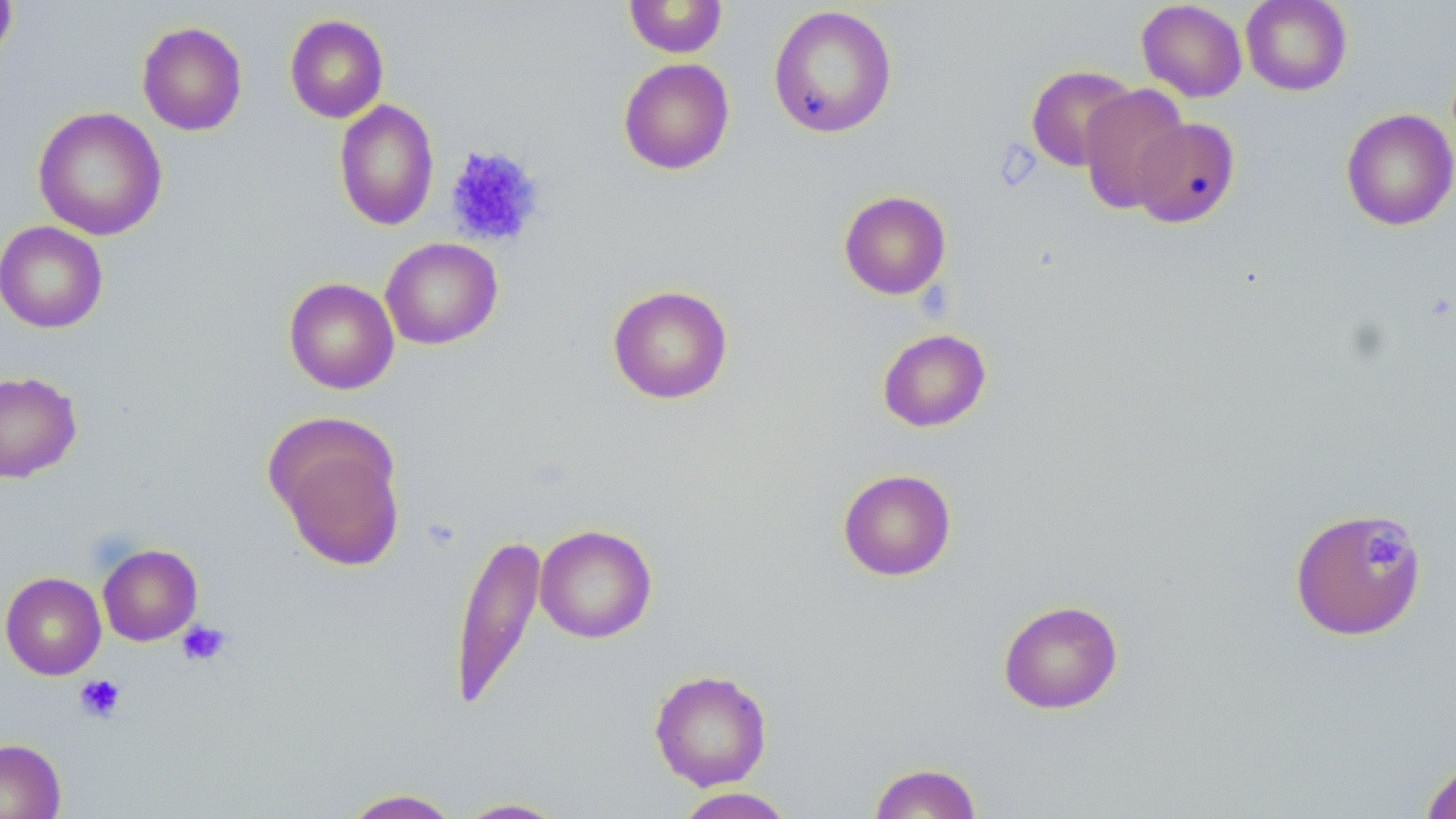 Approximate bounding boxes as (x1,y1)-(x2,y2) corner pairs in pixels. Platelet locations: (443,145)-(544,248), (1361,525)-(1409,574), (175,620)-(232,666), (75,674)-(125,723). Uninfected red blood cell locations: (0,0)-(18,63), (1241,0)-(1352,96), (624,1)-(728,58), (1136,1)-(1248,102), (768,5)-(897,138), (284,14)-(388,123), (136,21)-(248,136), (618,58)-(735,175), (1025,65)-(1138,172), (1078,84)-(1190,214), (334,99)-(439,231), (32,106)-(167,241), (1340,108)-(1456,231), (1129,118)-(1241,228), (839,190)-(951,299), (0,221)-(108,333), (380,237)-(503,349), (283,277)-(400,395), (607,284)-(733,404), (877,328)-(991,432), (0,370)-(82,483), (269,425)-(406,572), (837,468)-(957,581), (1289,506)-(1428,641), (535,524)-(657,643), (449,533)-(546,711), (98,543)-(202,646), (1,571)-(106,679), (998,599)-(1124,714), (649,668)-(773,791), (0,738)-(66,819), (1419,757)-(1456,819), (868,761)-(983,819), (672,787)-(796,818), (340,788)-(462,818), (452,797)-(571,818). Slide-level diagnosis: no evidence of blood parasites. Thin blood film. Image is 1456×819 pixels. One field of a larger specimen. May-Grünwald-Giemsa-stained preparation. 1000x magnification. Light microscopy.